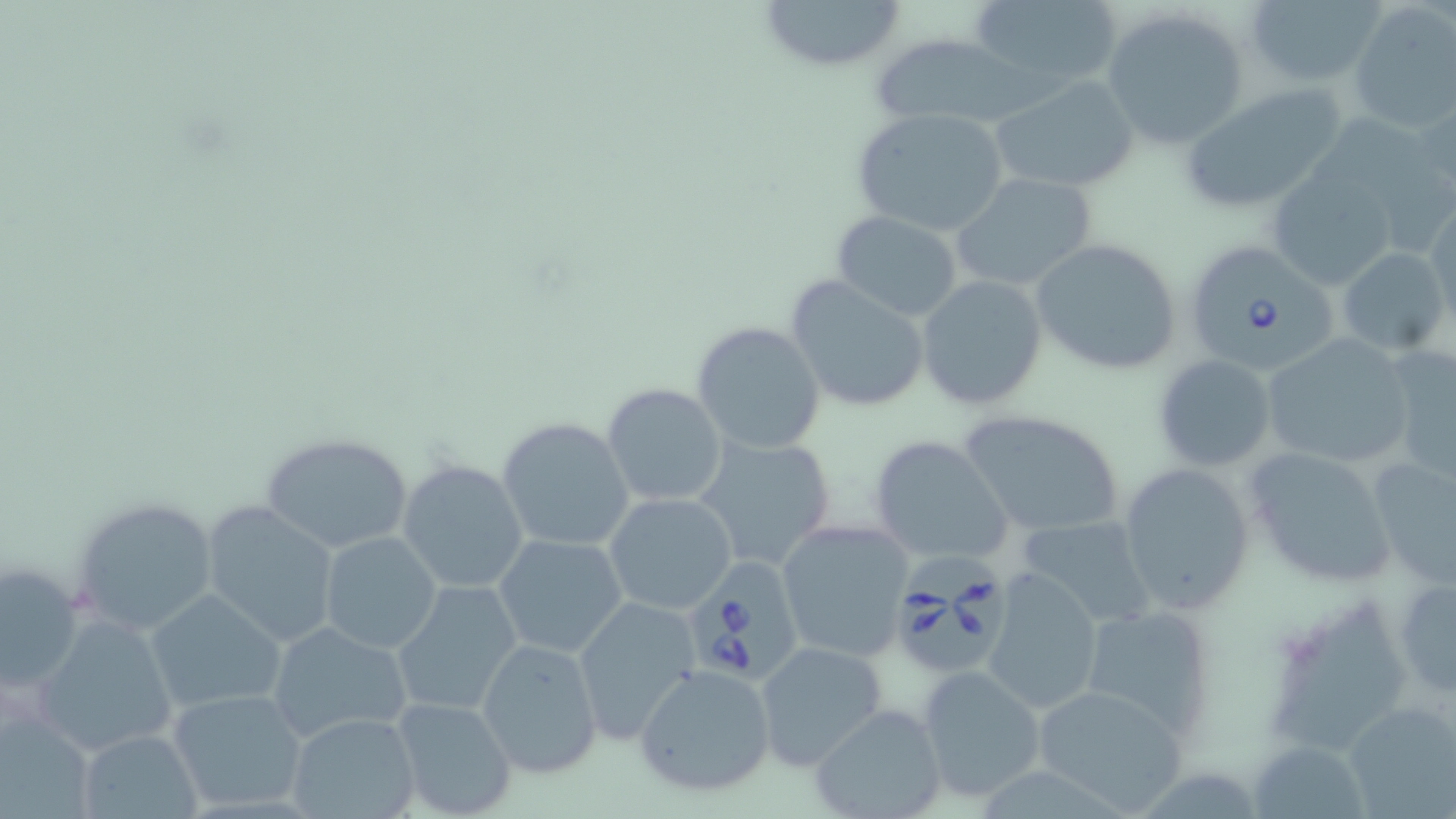
Approximate bounding boxes as (x1, y1, x2, y2) in pixels. Babesia divergens-infected red blood cell locations: (1188, 241, 1343, 372), (893, 548, 1014, 675), (681, 559, 807, 688). Uninfected red blood cell locations: (753, 0, 908, 74), (968, 0, 1125, 93), (1244, 0, 1385, 87), (1350, 5, 1455, 135), (1102, 9, 1250, 149), (869, 35, 1038, 130), (990, 74, 1139, 194), (1177, 82, 1347, 214), (1415, 92, 1455, 199), (850, 107, 1010, 237), (1268, 170, 1399, 292), (950, 172, 1099, 293), (1424, 202, 1456, 325), (831, 210, 963, 320), (1029, 237, 1182, 377), (1336, 248, 1452, 357), (785, 274, 931, 414), (916, 275, 1048, 412), (690, 321, 826, 455), (1257, 333, 1417, 471), (1381, 344, 1456, 483), (1152, 355, 1278, 471), (601, 382, 728, 507), (957, 410, 1128, 539), (497, 416, 634, 552), (259, 431, 416, 555), (692, 432, 839, 574), (867, 436, 1014, 567), (1243, 446, 1398, 591), (1365, 455, 1456, 589), (396, 458, 529, 596), (1118, 462, 1255, 616), (603, 493, 738, 614), (69, 497, 221, 638), (202, 500, 344, 646), (1012, 515, 1157, 632), (776, 519, 915, 661), (319, 531, 441, 653), (493, 533, 628, 659), (2, 561, 86, 694), (980, 568, 1107, 718), (1394, 574, 1456, 699), (392, 579, 525, 717), (146, 589, 287, 714), (1270, 594, 1421, 758), (572, 597, 703, 742), (1078, 604, 1216, 738), (31, 613, 180, 757), (266, 619, 412, 745), (475, 638, 605, 779), (754, 639, 888, 771), (634, 665, 777, 799), (914, 666, 1047, 804), (1032, 682, 1190, 813), (168, 688, 308, 813), (390, 693, 519, 819), (1342, 701, 1456, 816), (809, 703, 949, 819), (1, 709, 97, 818), (286, 711, 422, 819), (75, 729, 203, 819), (1247, 735, 1364, 819). Slide-level diagnosis: Babesia divergens. Thin blood film. Image is 1456×819 pixels. 1000x magnification. Single field of view. May-Grünwald-Giemsa-stained preparation. Light microscopy.